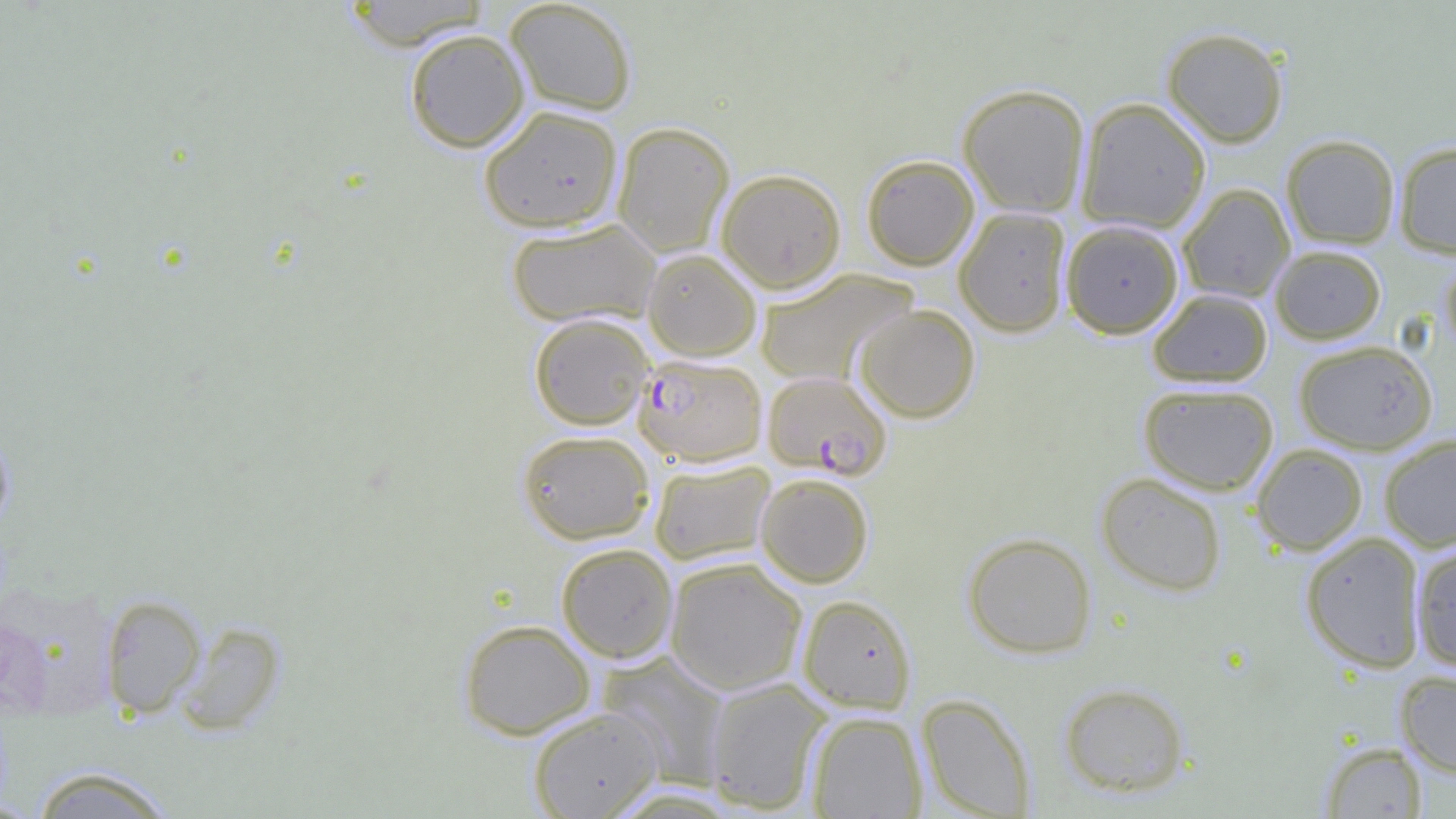

slide-level diagnosis = Plasmodium falciparum
field of view = single
preparation = thin blood film
uninfected red blood cell locations = approximate bounding boxes as (x1, y1, x2, y2) in pixels: (339, 0, 492, 50), (504, 0, 638, 116), (1161, 27, 1289, 148), (404, 28, 530, 152), (957, 83, 1091, 217), (1075, 97, 1211, 234), (478, 105, 624, 233), (611, 121, 735, 258), (1281, 134, 1400, 249), (1394, 141, 1456, 258), (861, 154, 980, 270), (716, 168, 847, 293), (1177, 183, 1295, 302), (954, 207, 1072, 337), (505, 218, 662, 328), (1061, 220, 1183, 338), (1270, 245, 1386, 344), (642, 248, 762, 360), (1440, 254, 1456, 359), (755, 268, 919, 386), (1148, 289, 1273, 387), (853, 304, 980, 423), (528, 312, 654, 430), (1294, 340, 1437, 454), (1138, 382, 1279, 495), (0, 422, 15, 536), (516, 429, 655, 544), (1379, 434, 1456, 552), (1251, 443, 1368, 556), (648, 459, 775, 566), (1096, 472, 1227, 596), (755, 473, 874, 587), (1299, 531, 1427, 672), (962, 532, 1097, 659), (1410, 540, 1456, 670), (556, 542, 678, 663), (664, 557, 807, 695), (100, 594, 206, 719), (797, 595, 916, 714), (458, 619, 596, 739), (174, 621, 287, 735), (597, 652, 731, 789), (1395, 670, 1456, 778), (704, 678, 832, 813), (1059, 682, 1190, 798), (917, 693, 1036, 818), (528, 707, 663, 819), (806, 711, 927, 818), (1320, 741, 1428, 818), (28, 765, 178, 818), (602, 786, 745, 818)
image size = 1456×819 pixels
magnification = 1000x
modality = light microscopy
Plasmodium falciparum-infected red blood cell locations = approximate bounding boxes as (x1, y1, x2, y2) in pixels: (633, 353, 767, 466), (762, 370, 892, 480)